Locate and identify every blood parasite.
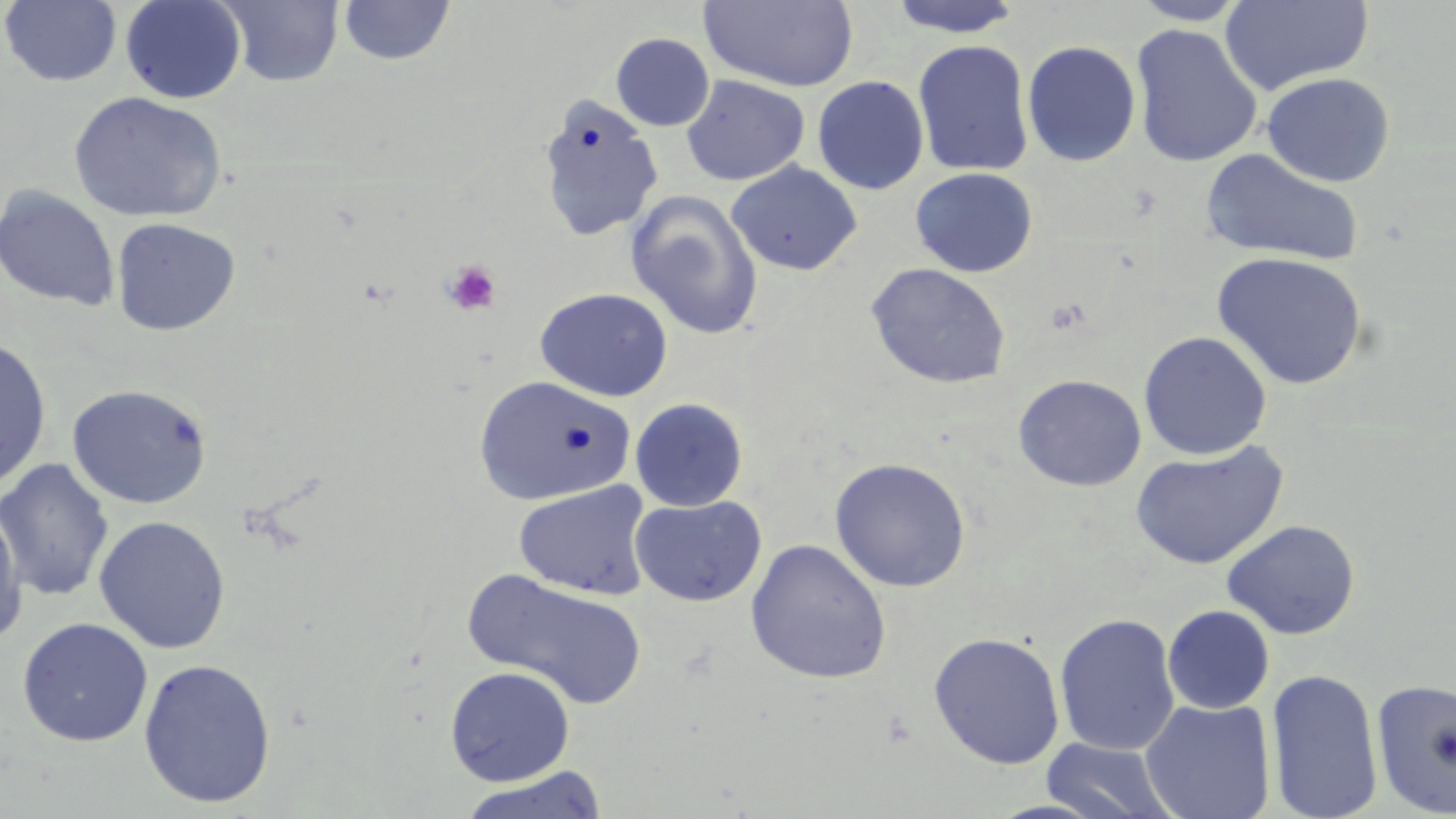

No blood parasites seen.

slide-level diagnosis = no evidence of blood parasites
uninfected red blood cell locations = approximate bounding boxes as [x1, y1, x2, y2] in pixels: [120, 0, 247, 104], [216, 0, 345, 87], [885, 0, 1026, 38], [1129, 0, 1251, 25], [1220, 0, 1374, 95], [0, 1, 122, 87], [339, 1, 456, 66], [701, 1, 858, 92], [1128, 24, 1263, 168], [610, 33, 715, 131], [912, 40, 1035, 177], [1021, 40, 1141, 167], [1261, 72, 1395, 187], [681, 75, 810, 186], [813, 76, 929, 194], [68, 90, 227, 223], [538, 95, 663, 242], [1201, 148, 1365, 267], [727, 161, 862, 276], [910, 167, 1038, 278], [0, 185, 121, 312], [625, 190, 763, 341], [111, 217, 241, 336], [1211, 252, 1369, 390], [865, 262, 1011, 389], [534, 287, 673, 401], [1138, 331, 1273, 460], [0, 336, 52, 490], [1012, 374, 1146, 491], [474, 375, 636, 506], [67, 384, 213, 509], [629, 397, 748, 511], [1130, 442, 1288, 569], [0, 457, 114, 602], [829, 457, 971, 592], [513, 481, 653, 600], [630, 495, 767, 607], [0, 499, 28, 647], [93, 515, 231, 653], [1221, 519, 1360, 640], [745, 539, 892, 684], [464, 569, 647, 710], [1162, 605, 1275, 714], [1054, 612, 1181, 757], [17, 617, 154, 747], [928, 632, 1066, 769], [138, 658, 276, 808], [444, 665, 576, 786], [1266, 668, 1384, 819], [1370, 678, 1456, 818], [1139, 698, 1276, 819], [1040, 737, 1180, 819], [455, 766, 610, 819]
preparation = thin blood smear
image size = 1456×819 pixels
platelet locations = approximate bounding boxes as [x1, y1, x2, y2] in pixels: [441, 260, 502, 316]
modality = optical microscopy
field of view = one of a larger specimen
stain = May-Grünwald-Giemsa
magnification = 1000x